State which parasite is depicted.
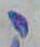

This is Toxoplasma gondii.

Micrograph. Captured at 1000x magnification.